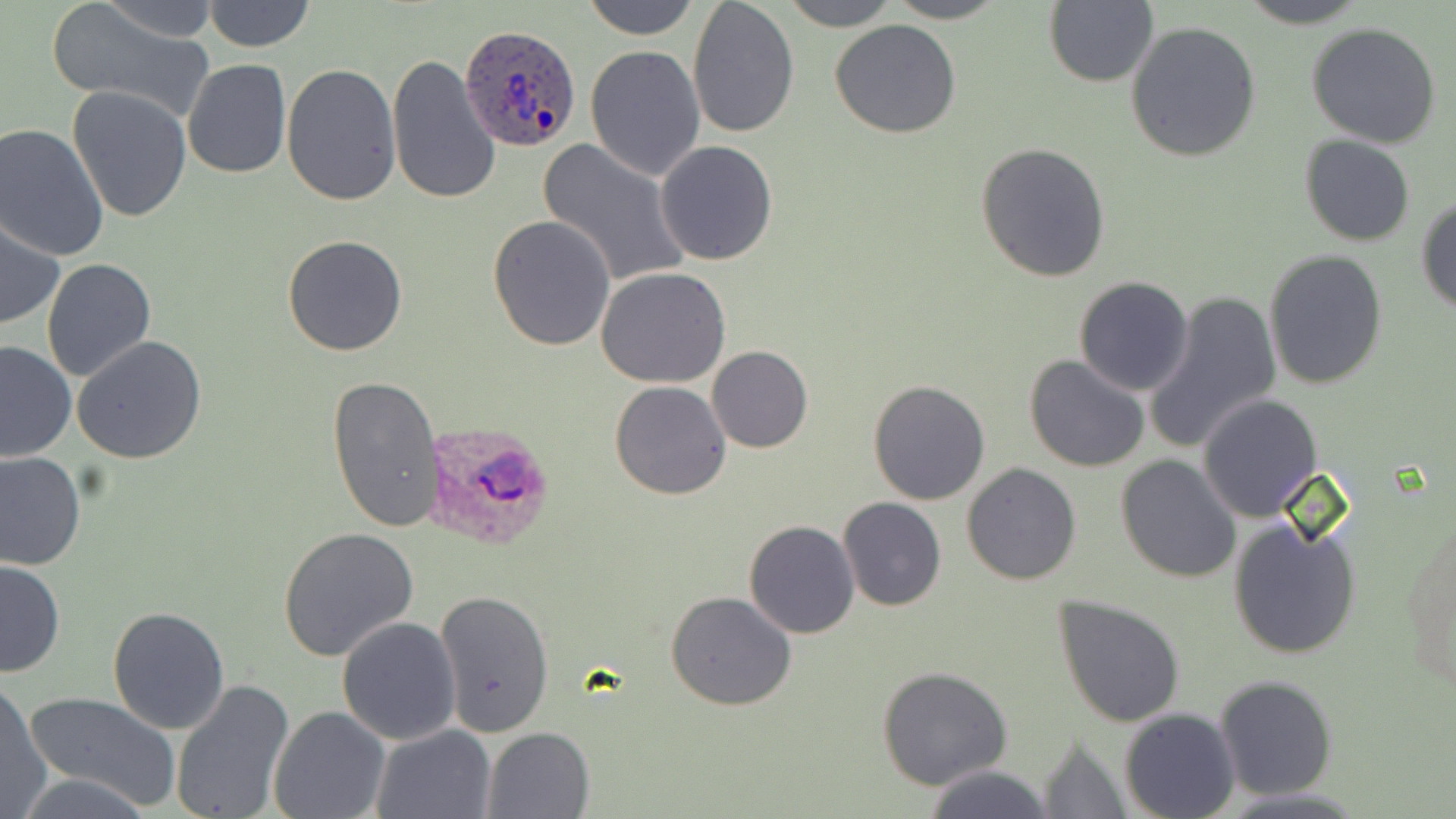
Approximate bounding boxes as named x1/y1/x2/y2 corners in pixels. Plasmodium ovale-infected red blood cell locations: (x1=460, y1=25, x2=582, y2=153), (x1=425, y1=422, x2=556, y2=549). Uninfected red blood cell locations: (x1=100, y1=0, x2=218, y2=44), (x1=584, y1=0, x2=697, y2=40), (x1=687, y1=0, x2=800, y2=140), (x1=781, y1=0, x2=901, y2=30), (x1=885, y1=0, x2=1009, y2=23), (x1=1233, y1=0, x2=1376, y2=27), (x1=203, y1=1, x2=315, y2=52), (x1=1043, y1=2, x2=1157, y2=87), (x1=45, y1=3, x2=217, y2=122), (x1=829, y1=19, x2=961, y2=139), (x1=1125, y1=21, x2=1262, y2=162), (x1=1304, y1=22, x2=1444, y2=148), (x1=585, y1=45, x2=706, y2=181), (x1=386, y1=53, x2=501, y2=206), (x1=181, y1=58, x2=291, y2=178), (x1=280, y1=63, x2=402, y2=205), (x1=68, y1=87, x2=191, y2=223), (x1=0, y1=124, x2=109, y2=261), (x1=1300, y1=135, x2=1415, y2=245), (x1=537, y1=139, x2=692, y2=290), (x1=655, y1=141, x2=778, y2=265), (x1=974, y1=143, x2=1112, y2=283), (x1=1417, y1=195, x2=1456, y2=315), (x1=488, y1=215, x2=616, y2=352), (x1=1, y1=218, x2=66, y2=332), (x1=281, y1=235, x2=409, y2=357), (x1=1263, y1=250, x2=1388, y2=389), (x1=41, y1=259, x2=158, y2=384), (x1=597, y1=267, x2=730, y2=387), (x1=1072, y1=275, x2=1195, y2=396), (x1=1143, y1=290, x2=1281, y2=453), (x1=71, y1=337, x2=207, y2=464), (x1=0, y1=340, x2=78, y2=462), (x1=707, y1=346, x2=813, y2=453), (x1=1024, y1=354, x2=1150, y2=474), (x1=326, y1=374, x2=444, y2=535), (x1=867, y1=379, x2=993, y2=505), (x1=608, y1=381, x2=731, y2=501), (x1=1198, y1=394, x2=1324, y2=522), (x1=0, y1=452, x2=84, y2=571), (x1=1115, y1=454, x2=1242, y2=582), (x1=961, y1=462, x2=1082, y2=584), (x1=837, y1=497, x2=946, y2=611), (x1=1403, y1=514, x2=1455, y2=702), (x1=1229, y1=516, x2=1361, y2=660), (x1=744, y1=519, x2=860, y2=639), (x1=277, y1=527, x2=419, y2=660), (x1=0, y1=558, x2=64, y2=678), (x1=434, y1=589, x2=554, y2=739), (x1=666, y1=590, x2=798, y2=711), (x1=1053, y1=595, x2=1187, y2=727), (x1=107, y1=605, x2=232, y2=734), (x1=337, y1=617, x2=462, y2=744), (x1=877, y1=667, x2=1013, y2=792), (x1=1213, y1=673, x2=1338, y2=801), (x1=0, y1=678, x2=50, y2=817), (x1=170, y1=678, x2=295, y2=819), (x1=21, y1=690, x2=183, y2=812), (x1=268, y1=705, x2=390, y2=819), (x1=1119, y1=707, x2=1239, y2=819), (x1=369, y1=723, x2=495, y2=819), (x1=482, y1=726, x2=596, y2=818), (x1=1035, y1=735, x2=1135, y2=818), (x1=922, y1=765, x2=1055, y2=819), (x1=16, y1=771, x2=158, y2=818). Slide-level diagnosis: Plasmodium ovale. Single field of view. Thin blood smear. May-Grünwald-Giemsa stain. Image is 1456×819 pixels. Captured at 1000x magnification. Optical microscopy.